State the blood parasite species.
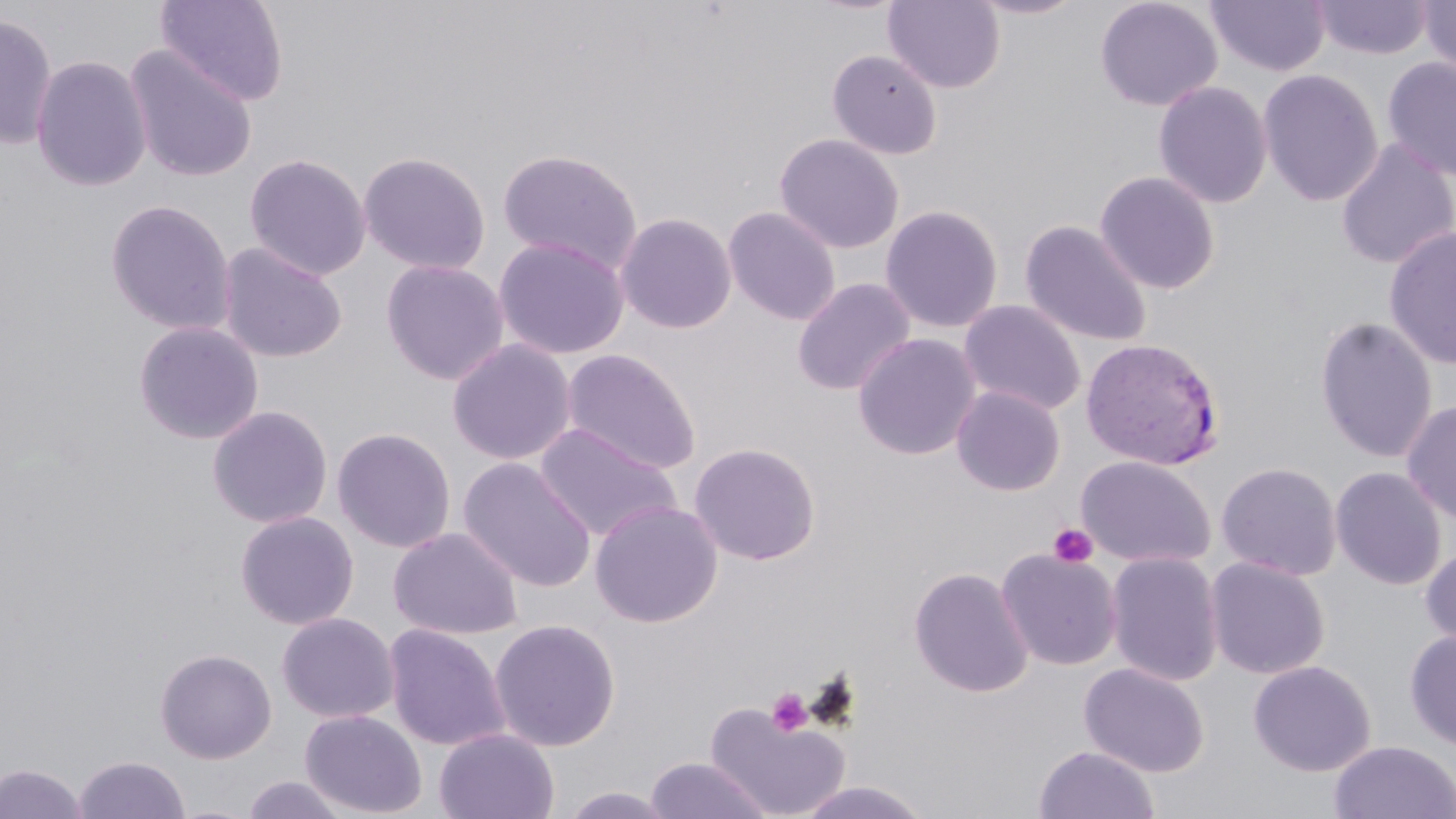
Plasmodium vivax.

Approximate bounding boxes as (x1,y1)-(x2,y2) corner pairs in pixels. Plasmodium vivax-infected red blood cell locations: (1080,336)-(1225,470). Uninfected red blood cell locations: (156,0)-(289,106), (883,0)-(1005,93), (968,0)-(1088,20), (1094,0)-(1223,112), (1206,0)-(1330,77), (1312,0)-(1433,60), (1417,1)-(1456,78), (0,14)-(58,151), (124,46)-(258,183), (827,48)-(942,160), (1383,54)-(1456,180), (30,55)-(152,192), (1258,69)-(1384,207), (1153,80)-(1273,208), (774,133)-(904,254), (1335,140)-(1456,270), (496,147)-(643,275), (357,151)-(491,274), (244,152)-(371,281), (1095,171)-(1220,294), (105,199)-(236,335), (880,204)-(1003,333), (722,206)-(841,325), (615,212)-(737,334), (1019,219)-(1153,347), (1383,225)-(1456,371), (493,236)-(630,360), (217,242)-(347,363), (380,258)-(509,385), (792,277)-(916,396), (959,300)-(1087,416), (1314,315)-(1437,464), (132,320)-(265,445), (852,332)-(981,460), (446,338)-(577,465), (561,348)-(701,474), (951,386)-(1065,496), (1401,398)-(1456,526), (207,405)-(333,528), (535,423)-(682,542), (331,426)-(456,552), (688,442)-(821,565), (1076,455)-(1216,569), (458,457)-(597,592), (1216,462)-(1342,581), (1331,466)-(1446,590), (589,499)-(723,627), (234,511)-(359,630), (387,527)-(523,640), (1419,544)-(1456,653), (997,548)-(1122,670), (1105,552)-(1224,687), (1206,557)-(1330,680), (908,566)-(1034,697), (276,612)-(399,723), (489,618)-(621,752), (383,623)-(510,750), (1404,629)-(1456,751), (155,647)-(277,763), (1248,660)-(1376,776), (1079,662)-(1210,777), (704,702)-(849,818), (299,709)-(427,818), (434,727)-(560,819), (1328,740)-(1455,819), (1034,745)-(1160,819), (73,755)-(190,819), (644,756)-(773,819), (0,763)-(88,819), (240,774)-(352,818), (796,781)-(933,819), (559,786)-(679,818). Platelet locations: (1048,523)-(1099,569), (765,687)-(813,737). May-Grünwald-Giemsa stain. Image is 1456×819 pixels. Thin blood smear. One field of a larger specimen. Light microscopy. 1000x magnification.